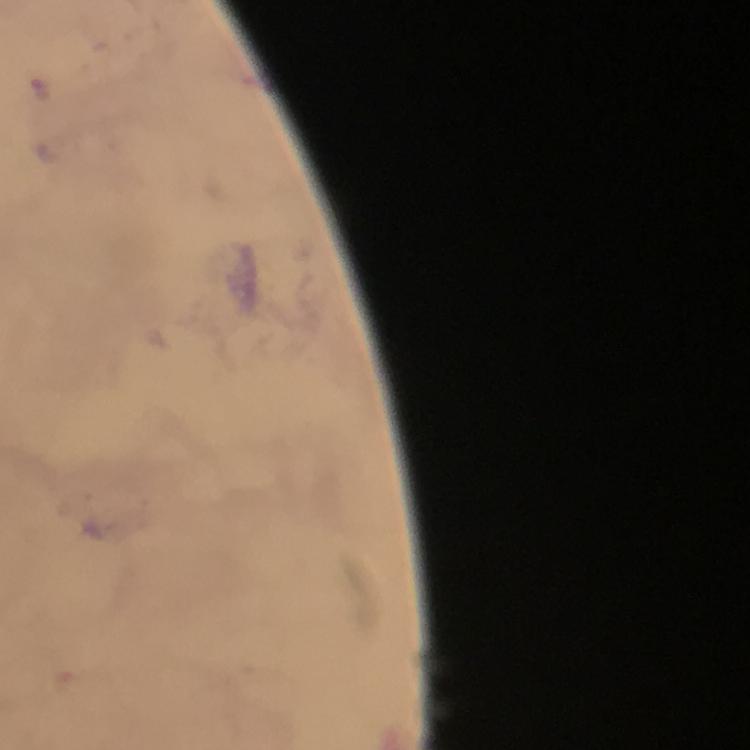

Approximate centers as [x, y] in pixels.
Summary:
  - Plasmodium parasite locations: [43, 88]
  - Preparation: thick blood smear
  - Magnification: 100x
  - Immersion oil: used
  - Image size: 750×750 pixels
  - Capture: smartphone mounted on the microscope
  - Context: from a malaria diagnostic workup
  - Stain: Giemsa
  - Cropped from: a single field of view